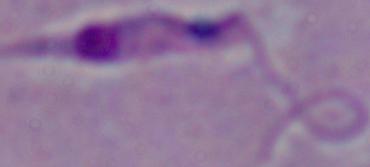

identification = Leishmania
modality = micrograph
magnification = 1000x